Describe the morphology of the red blood cells.
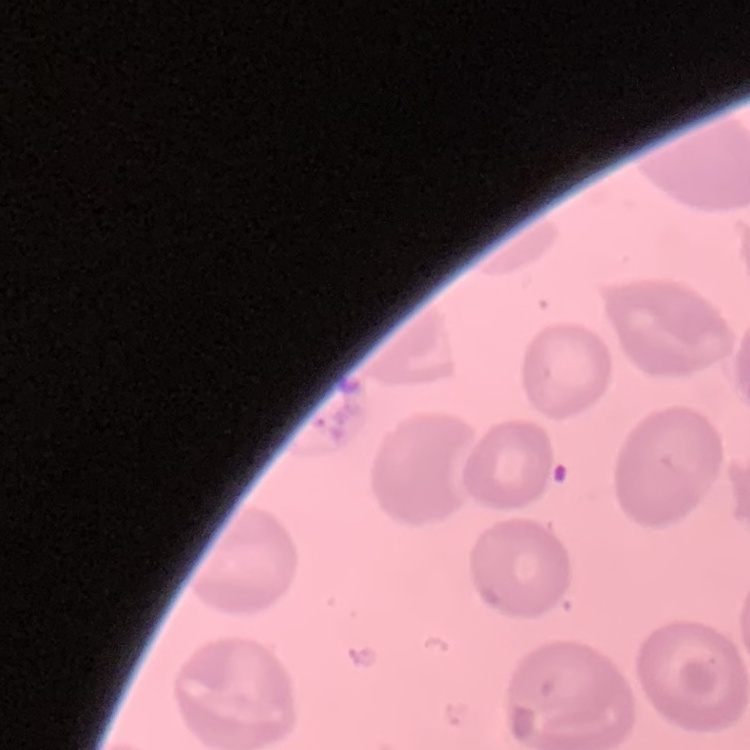
They show no rouleaux formation.

Thin blood smear. One tile cut from a larger photomicrograph. Field's or Giemsa stain.